Give the position of every Plasmodium parasite.
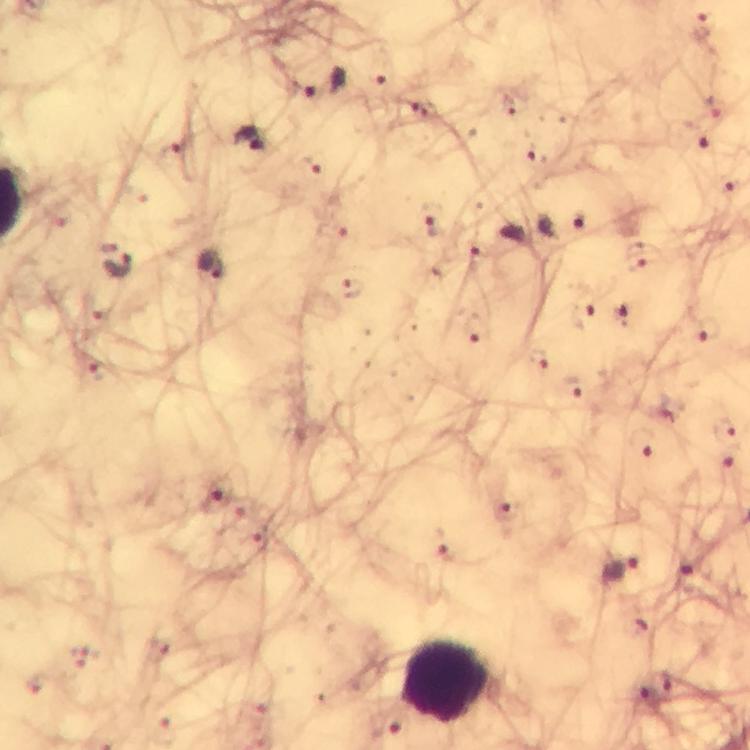

Approximate centers as [x, y] in pixels.
Plasmodium parasites: [703, 27], [323, 86], [506, 103], [422, 107], [248, 139], [708, 140], [171, 154], [535, 157], [309, 166], [724, 185], [579, 221], [433, 223], [477, 258], [116, 262], [210, 267], [350, 289], [621, 315], [584, 319], [477, 328], [706, 330], [537, 359], [97, 369], [573, 386], [727, 432], [648, 444], [727, 457], [217, 503], [503, 513], [257, 539], [442, 542], [621, 571], [688, 581], [669, 687], [644, 693].

Summary:
  - Leukocyte locations: [446, 683]
  - Magnification: 100x
  - Stain: Giemsa
  - Image size: 750×750 pixels
  - Capture: smartphone camera through the microscope
  - Cropped from: a single field of view
  - Immersion oil: applied
  - Context: from a diagnostic examination for malaria
  - Preparation: thick blood smear